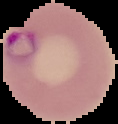
Summary:
  - Preparation: thin blood smear
  - Image size: 118×124 pixels
  - Image type: segmented cell region on a black background
  - Result: malaria parasites identified